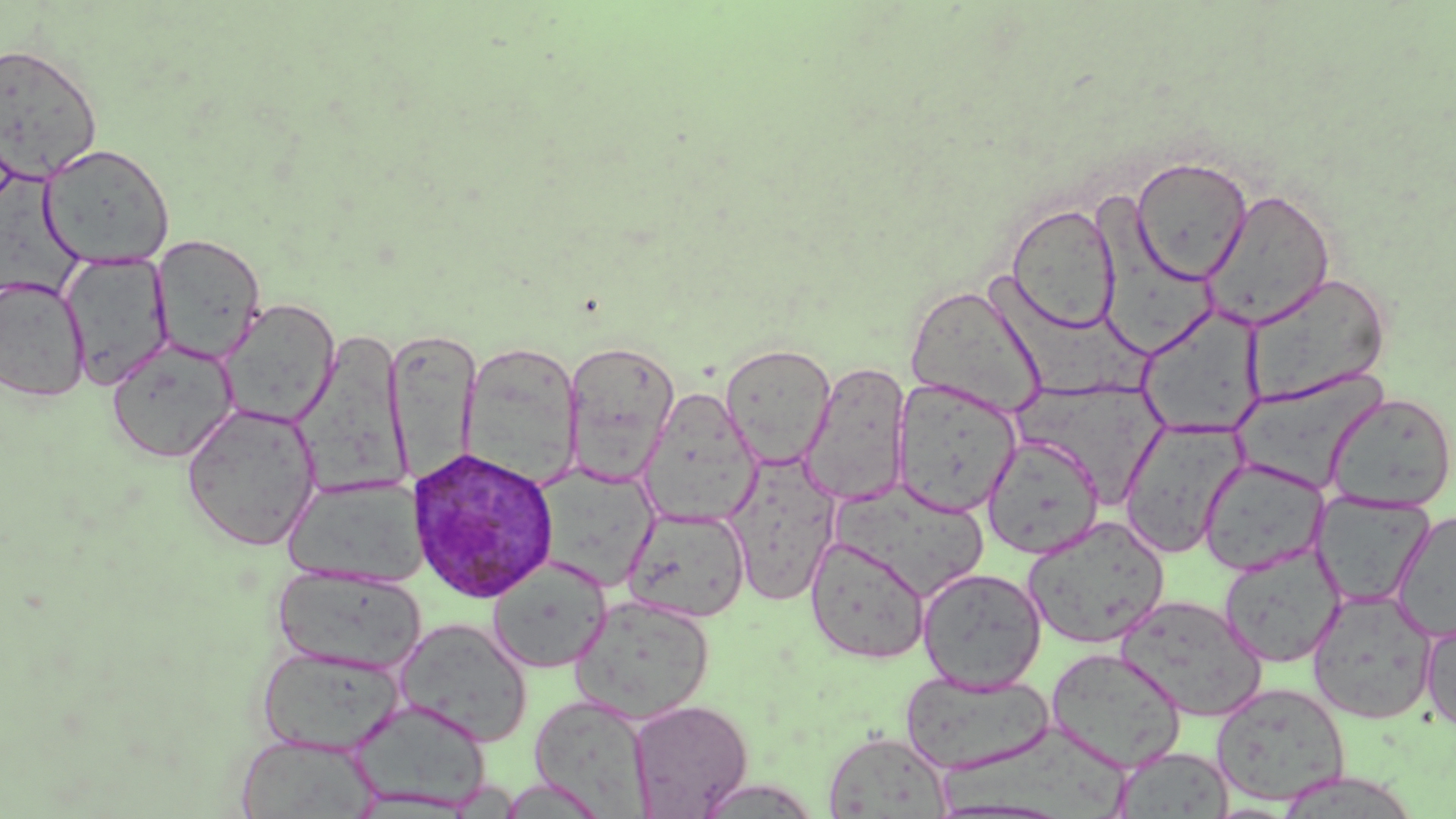
Summary:
  - Coordinate format: approximate bounding boxes as (x1,y1)-(x2,y2) corner pairs in pixels
  - Plasmodium ovale-infected red blood cell locations: (408,445)-(560,604)
  - Uninfected red blood cell locations: (0,42)-(103,182), (39,143)-(175,269), (1131,156)-(1253,285), (3,172)-(88,302), (1201,188)-(1336,330), (1091,197)-(1220,361), (1007,203)-(1121,333), (151,234)-(266,365), (60,251)-(174,390), (984,269)-(1157,396), (1242,272)-(1391,407), (0,275)-(91,402), (905,284)-(1047,417), (218,299)-(340,428), (1138,307)-(1265,438), (295,327)-(412,497), (386,330)-(478,488), (106,338)-(238,463), (462,341)-(584,489), (563,341)-(681,485), (719,342)-(837,468), (799,361)-(911,507), (1231,371)-(1387,492), (892,378)-(1022,518), (1018,380)-(1167,505), (638,388)-(762,527), (1326,391)-(1456,510), (181,402)-(322,551), (1119,418)-(1246,558), (983,435)-(1103,559), (724,454)-(842,607), (1199,457)-(1328,576), (534,464)-(659,589), (284,476)-(429,588), (824,479)-(992,602), (1311,491)-(1436,608), (624,506)-(751,622), (1392,510)-(1456,640), (1023,516)-(1169,650), (806,536)-(930,664), (1219,544)-(1345,667), (487,558)-(612,673), (270,565)-(424,676), (917,566)-(1046,692), (1308,590)-(1438,724), (1116,594)-(1266,721), (570,595)-(716,723), (1421,617)-(1456,736), (395,618)-(533,747), (257,645)-(405,755), (1045,647)-(1186,772), (900,668)-(1055,776), (1211,682)-(1351,807), (529,694)-(654,816), (349,698)-(492,810), (627,699)-(752,817), (936,726)-(1133,818), (823,730)-(952,818), (236,734)-(380,818), (1114,745)-(1235,818), (496,776)-(609,819), (694,778)-(822,818)
  - Slide-level diagnosis: Plasmodium ovale
  - Image size: 1456×819 pixels
  - Modality: light microscopy
  - Preparation: thin blood smear
  - Magnification: 1000x
  - Stain: May-Grünwald-Giemsa
  - Field of view: one of a larger specimen